Point out each Plasmodium parasite.
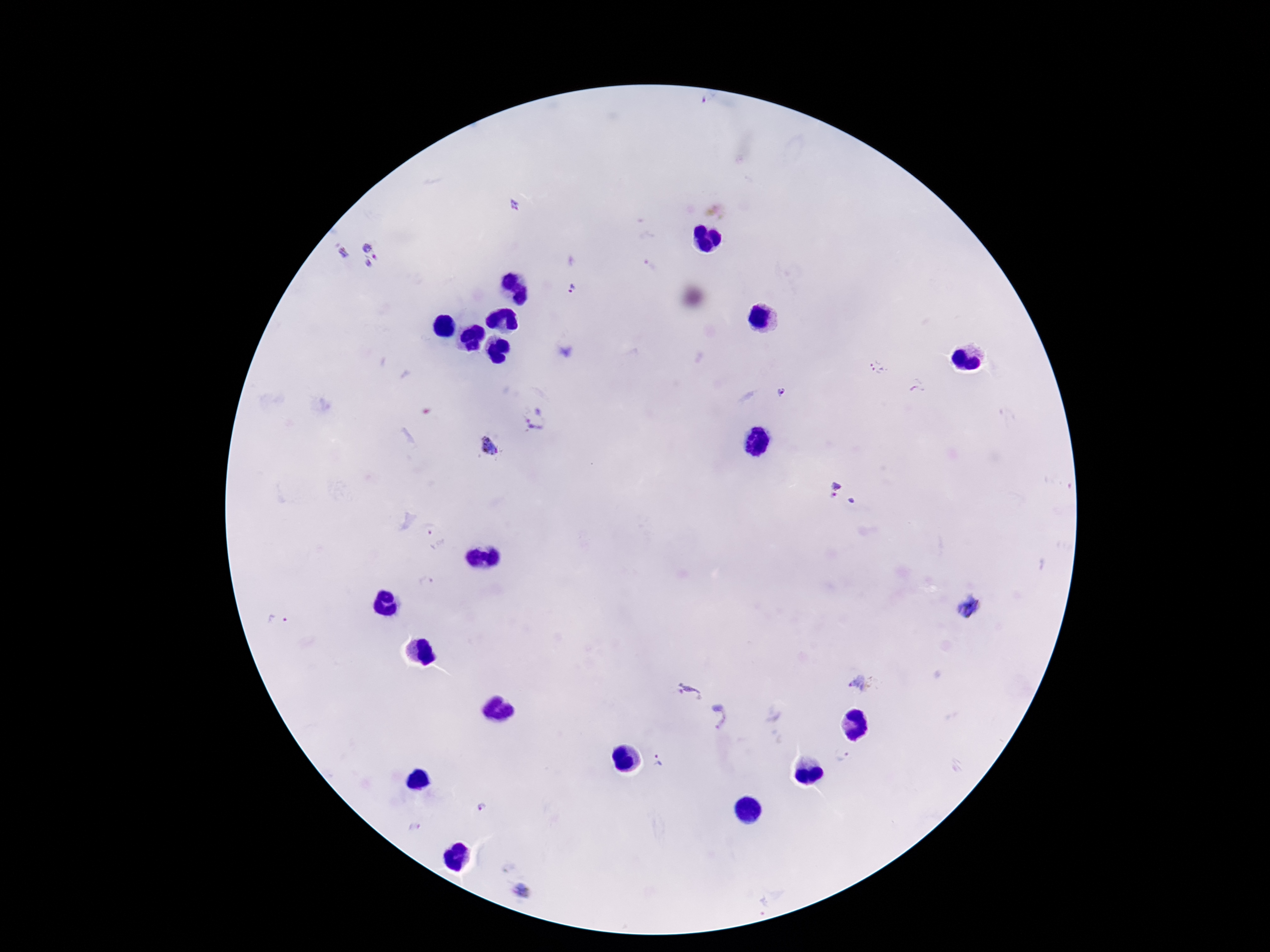
Approximate centers as {x, y} in pixels.
Plasmodium parasites: {708, 99}, {514, 204}, {342, 253}, {375, 254}, {651, 266}, {575, 291}, {878, 367}, {918, 388}, {782, 392}, {537, 419}, {489, 447}, {832, 489}, {852, 501}, {434, 535}, {424, 581}, {969, 607}, {277, 620}, {860, 684}, {689, 692}, {720, 717}, {844, 757}, {659, 764}, {480, 808}, {414, 830}, {522, 892}.

Patient malaria status: infected. Smartphone photograph taken through the microscope eyepiece. Image is 1270×952 pixels. Giemsa-stained preparation. Thick peripheral-blood smear. 100x magnification. Single field of view.